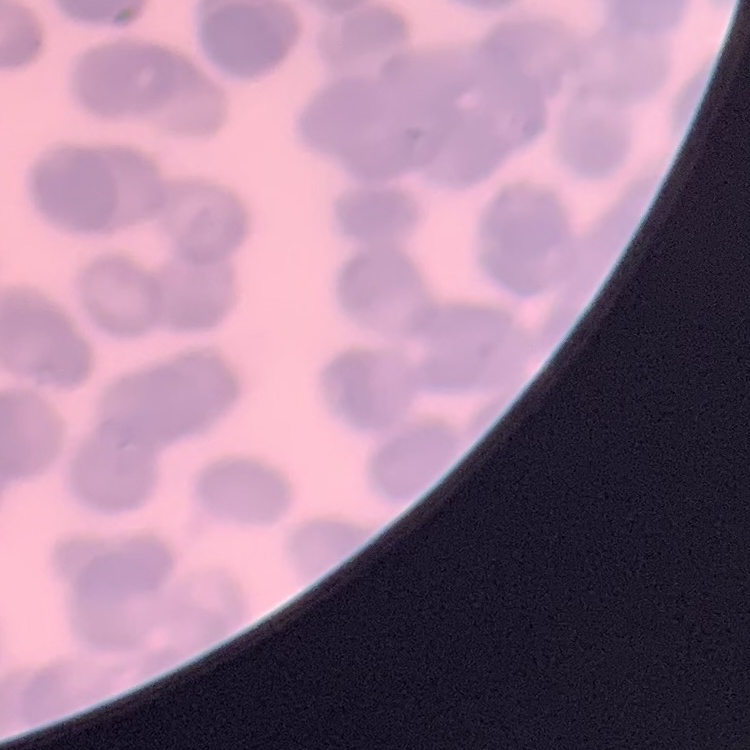
The red blood cells show rouleaux formation. Stained with either Field's or Giemsa. Thin peripheral smear. Square crop of a larger photomicrograph.